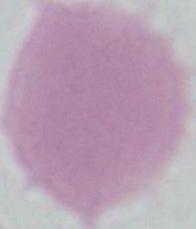

{
  "identification": "erythrocyte",
  "modality": "photomicrograph",
  "magnification": "1000x"
}